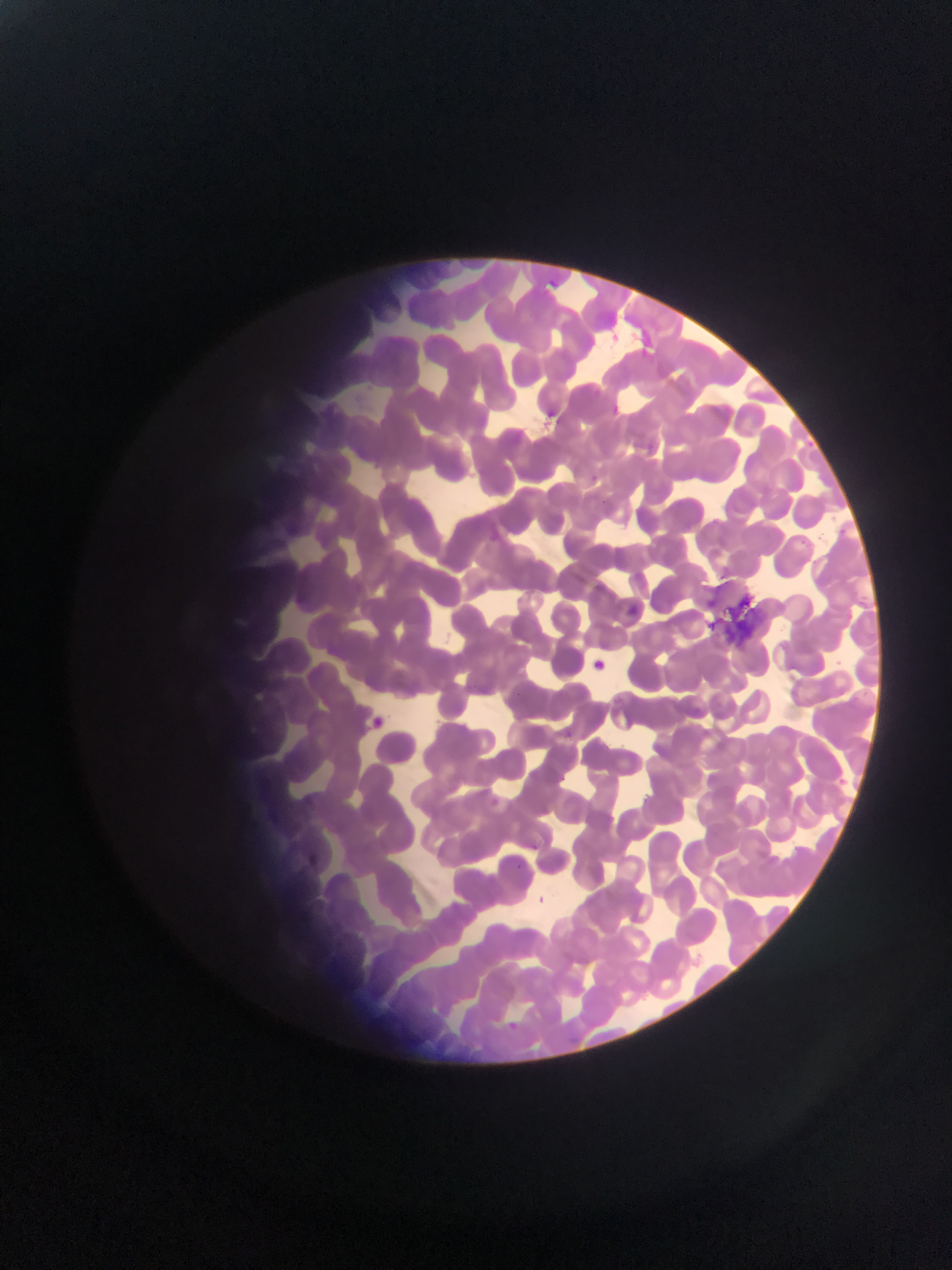

Approximate bounding boxes as {left, top, right, bottom} in pixels.
Summary:
  - Artifact (stain precipitate or debris) locations: {721, 591, 764, 645}
  - Plasmodium parasite locations: {626, 602, 637, 619}, {591, 655, 614, 672}, {374, 715, 390, 728}, {307, 852, 324, 867}
  - Country: Ghana
  - Preparation: thin blood smear
  - Field of view: single
  - Capture: mobile-phone photograph through a microscope
  - Image size: 952×1270 pixels